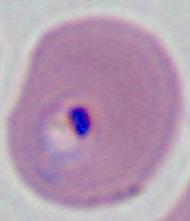

Summary:
  - Modality: micrograph
  - Identification: Plasmodium
  - Magnification: 400x or 1000x